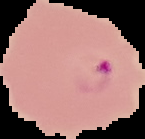

image type = cell region segmented out of the field of view; surrounding area masked to black
malaria status = parasitized
image size = 145×139 pixels
preparation = thin blood film